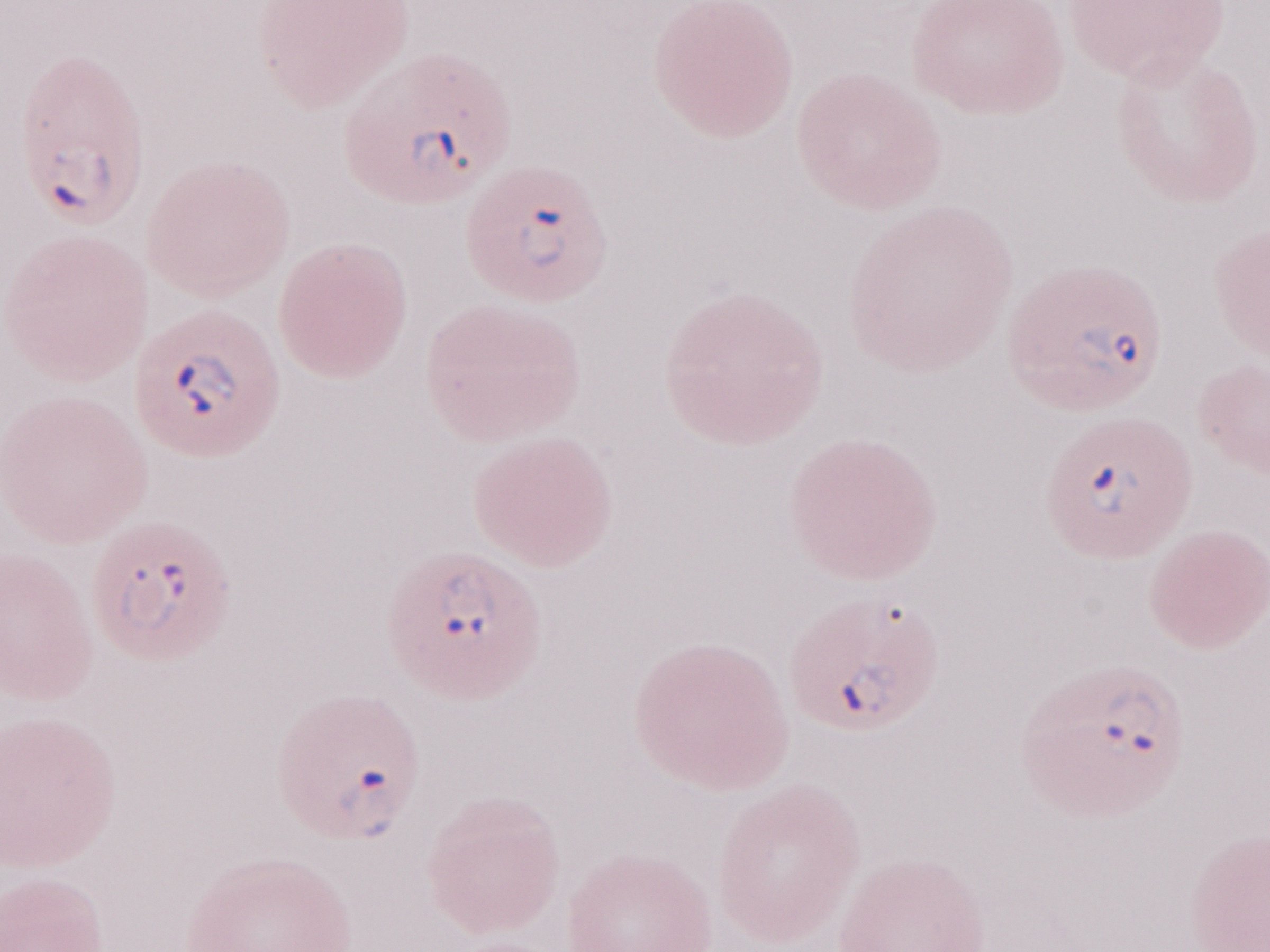 Olympus BX43 microscope and DP73 digital camera. Magnification: 1,000x. Thin blood smear. Patient-level malaria diagnosis: positive. One field of this slide. Image is 1270×952 pixels. May-Grünwald-Giemsa stain.